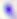

Summary:
  - Identification: Toxoplasma gondii
  - Modality: micrograph
  - Magnification: 400x